Point out each leukocyte.
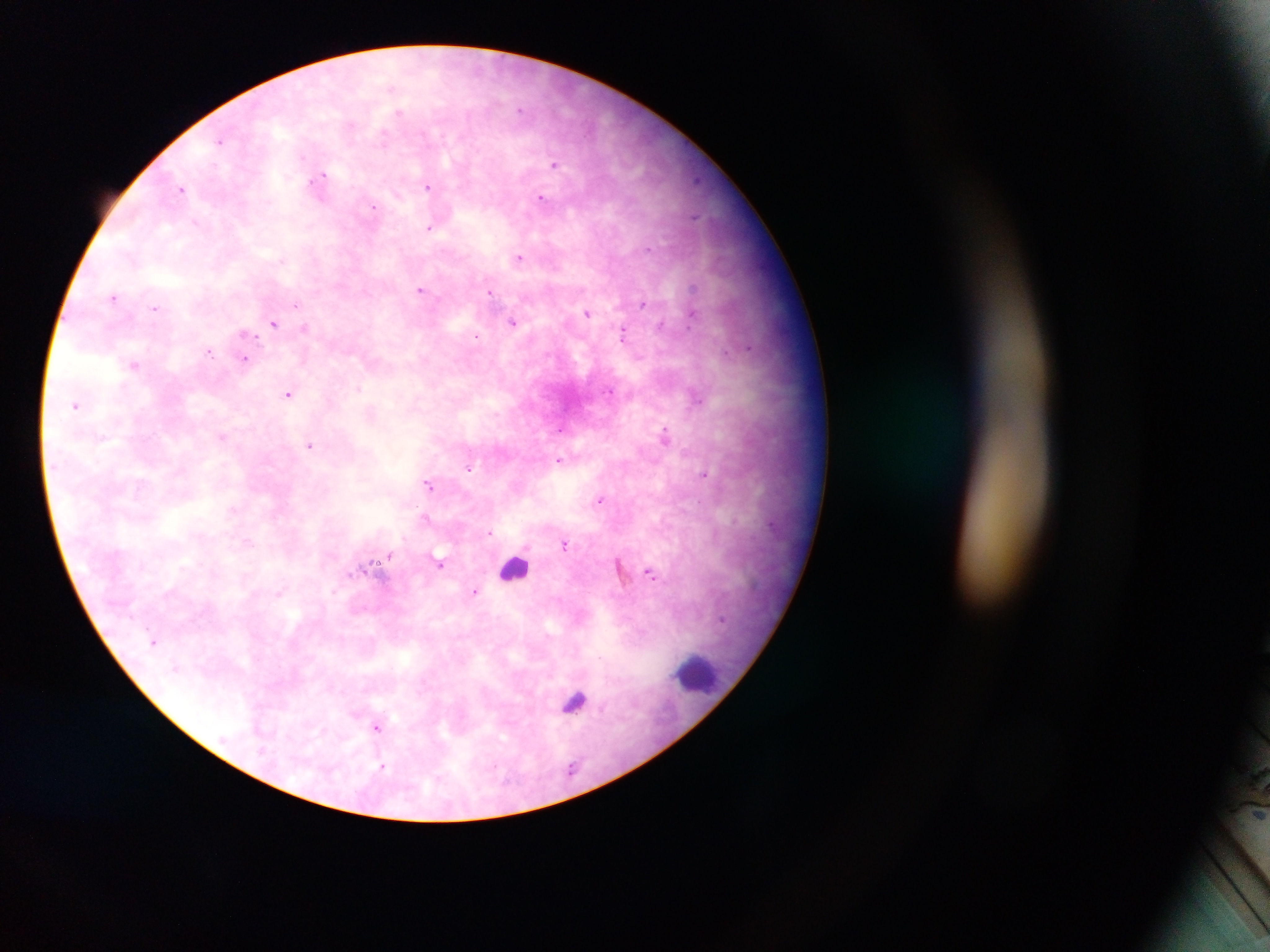

Approximate centers as {x, y} in pixels.
Leukocytes: {515, 568}, {696, 673}, {572, 698}.

Malaria parasite locations: {522, 109}, {401, 113}, {384, 136}, {220, 141}, {554, 164}, {321, 181}, {430, 187}, {182, 189}, {542, 198}, {373, 207}, {430, 227}, {520, 257}, {422, 290}, {491, 291}, {115, 295}, {643, 303}, {156, 308}, {587, 313}, {693, 313}, {513, 321}, {274, 322}, {245, 332}, {624, 332}, {479, 336}, {750, 348}, {210, 351}, {244, 358}, {134, 364}, {290, 393}, {698, 395}, {76, 405}, {561, 429}, {665, 434}, {222, 436}, {309, 445}, {560, 460}, {468, 468}, {704, 475}, {429, 483}, {601, 500}, {233, 510}, {426, 519}, {491, 533}, {565, 544}, {389, 555}, {441, 564}, {366, 568}, {650, 572}, {476, 591}, {156, 641}, {378, 726}, {383, 767}. Thick blood smear. One field of view. Sample from Ghana. Image is 1270×952 pixels. Photographed through a microscope with a mobile-phone camera.